Give the position of every malaria parasite.
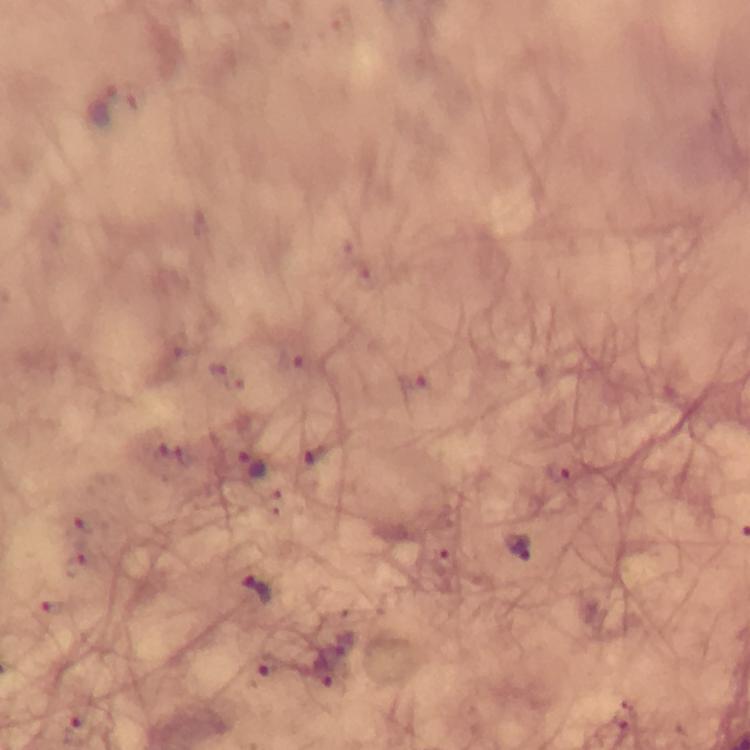

Approximate centers as (x, y) in pixels.
Malaria parasites: (251, 463), (558, 473), (519, 548), (257, 592), (268, 665).

Smartphone photograph taken through a microscope. Thick smear. Immersion oil applied. Giemsa-stained preparation. From a diagnostic examination for malaria. Image is 750×750 pixels. 100x magnification. A crop from one field of view.